Comment on the morphology of the red blood cells.
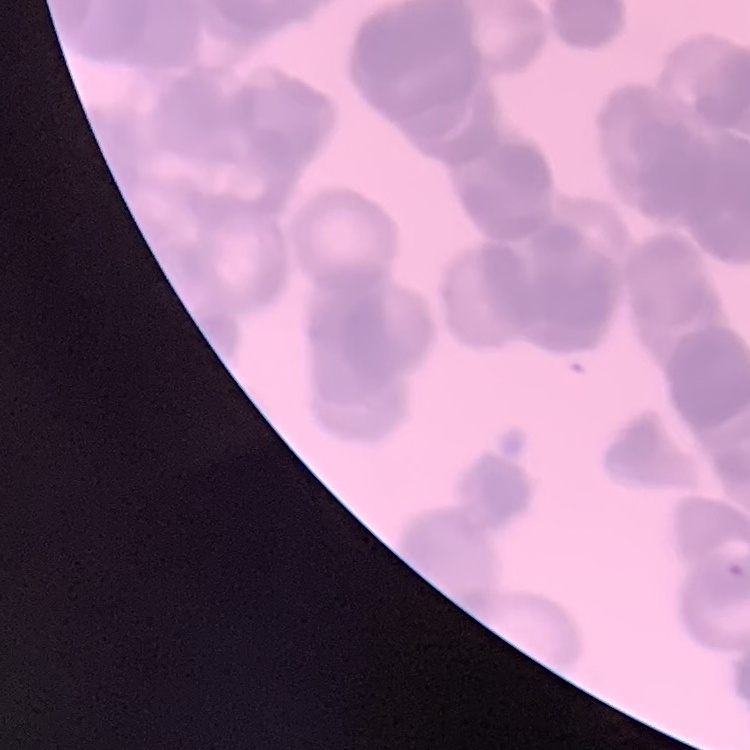
Rouleaux formation.

preparation = thin blood smear
stain = Field's or Giemsa
image type = one tile cut from a larger photomicrograph